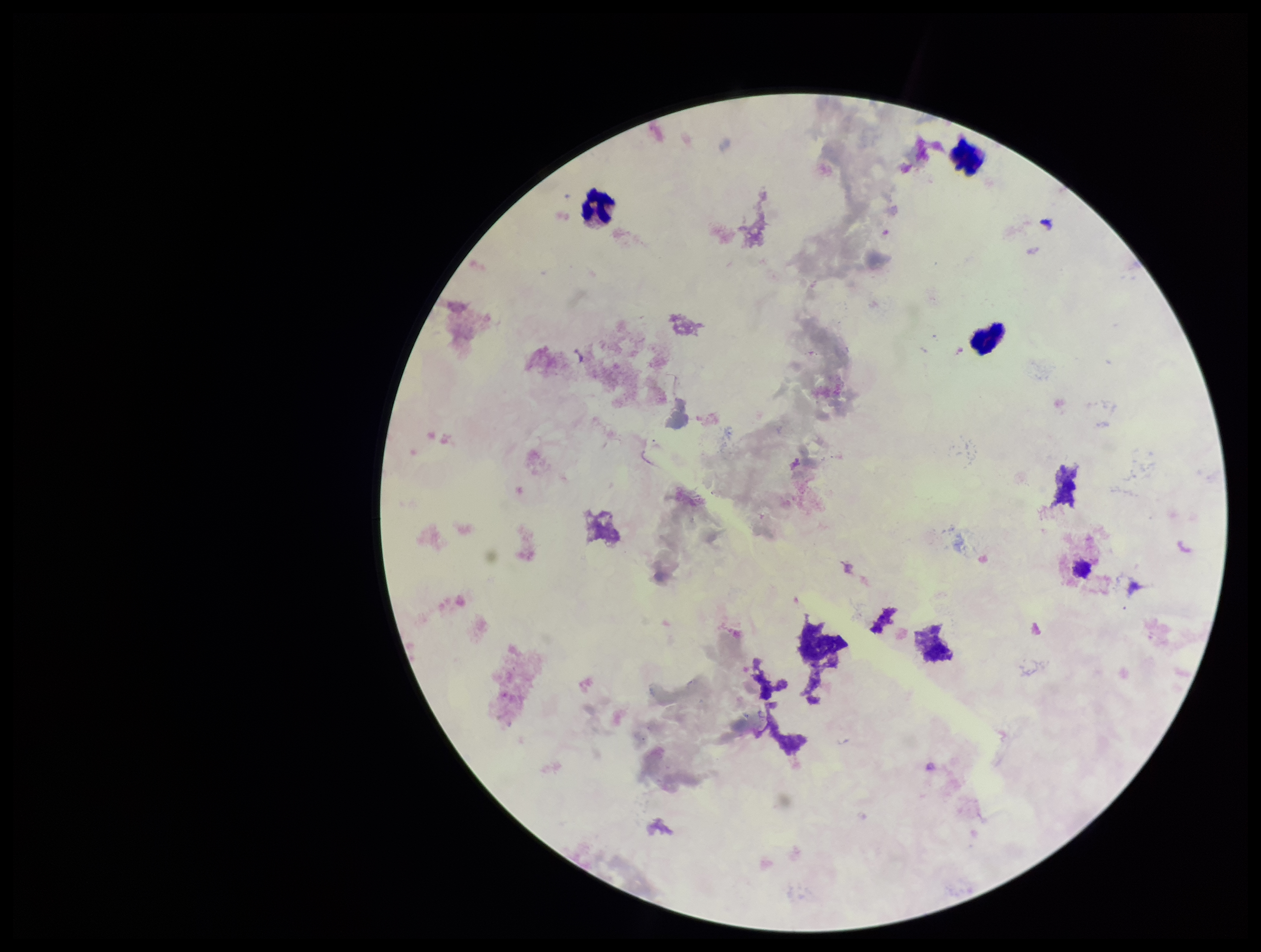
Summary:
  - Plasmodium parasites: none seen
  - Parasite count: 0
  - Patient malaria status: negative
  - Capture: smartphone photograph through the microscope eyepiece
  - Preparation: thick
  - Image size: 1261×952 pixels
  - Leukocyte count: 3
  - Stain: Giemsa
  - Field of view: one from this slide